Assess this cell for malaria.
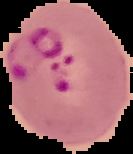

It is parasitized.

Summary:
  - Image type: cell region segmented out of the field of view; surrounding area masked to black
  - Image size: 133×154 pixels
  - Preparation: thin blood smear